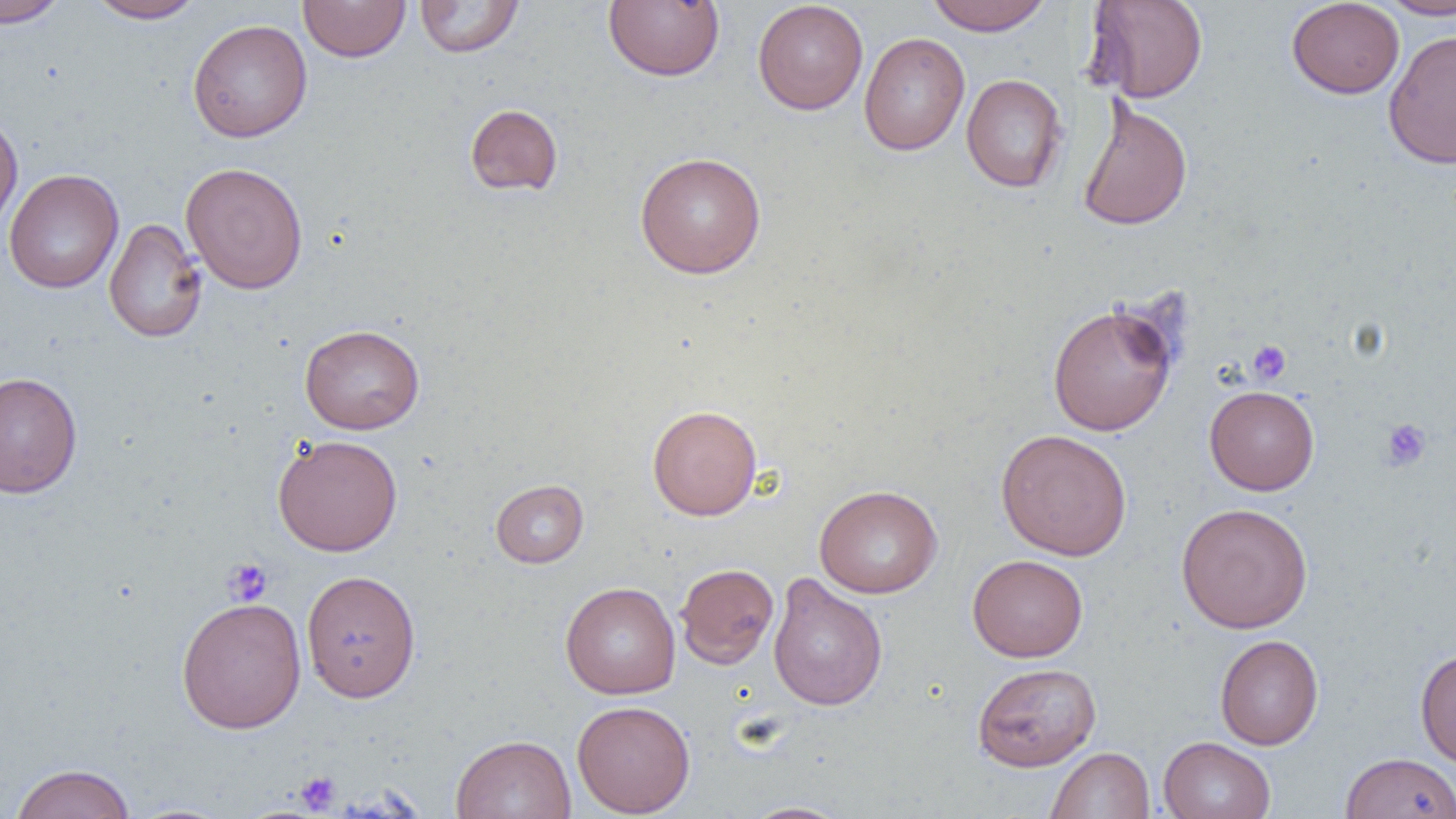
slide-level diagnosis = negative for blood parasites
modality = light microscopy
magnification = 1000x
uninfected red blood cell locations = approximate bounding boxes as (x1,y1)-(x2,y2) corner pairs in pixels: (0,0)-(70,28), (86,0)-(206,23), (298,0)-(411,62), (414,0)-(525,58), (603,0)-(725,81), (752,0)-(868,115), (925,0)-(1053,35), (1084,0)-(1209,103), (1375,0)-(1456,20), (1286,1)-(1405,99), (187,19)-(313,143), (1383,28)-(1456,169), (859,32)-(969,155), (960,74)-(1068,192), (1076,98)-(1193,232), (464,104)-(563,196), (0,114)-(23,238), (634,151)-(766,278), (181,162)-(308,294), (4,168)-(124,294), (104,217)-(208,343), (1047,301)-(1179,436), (299,324)-(424,434), (0,370)-(82,499), (1205,385)-(1320,495), (647,404)-(762,520), (996,428)-(1132,560), (272,434)-(403,556), (490,479)-(588,568), (814,484)-(942,598), (1175,502)-(1313,633), (967,554)-(1088,662), (675,563)-(779,669), (301,569)-(420,702), (768,573)-(888,711), (560,581)-(681,699), (176,597)-(307,733), (1215,634)-(1323,750), (1415,647)-(1456,769), (972,662)-(1101,771), (572,699)-(695,817), (450,733)-(576,819), (1158,736)-(1275,819), (1046,747)-(1155,819), (1341,752)-(1456,819), (10,763)-(135,818), (740,801)-(853,818), (122,803)-(240,819)
image size = 1456×819 pixels
field of view = single
preparation = thin blood film
platelet locations = approximate bounding boxes as (x1,y1)-(x2,y2) corner pairs in pixels: (1247,340)-(1291,385), (1381,419)-(1432,472), (223,558)-(273,605), (296,771)-(340,813)